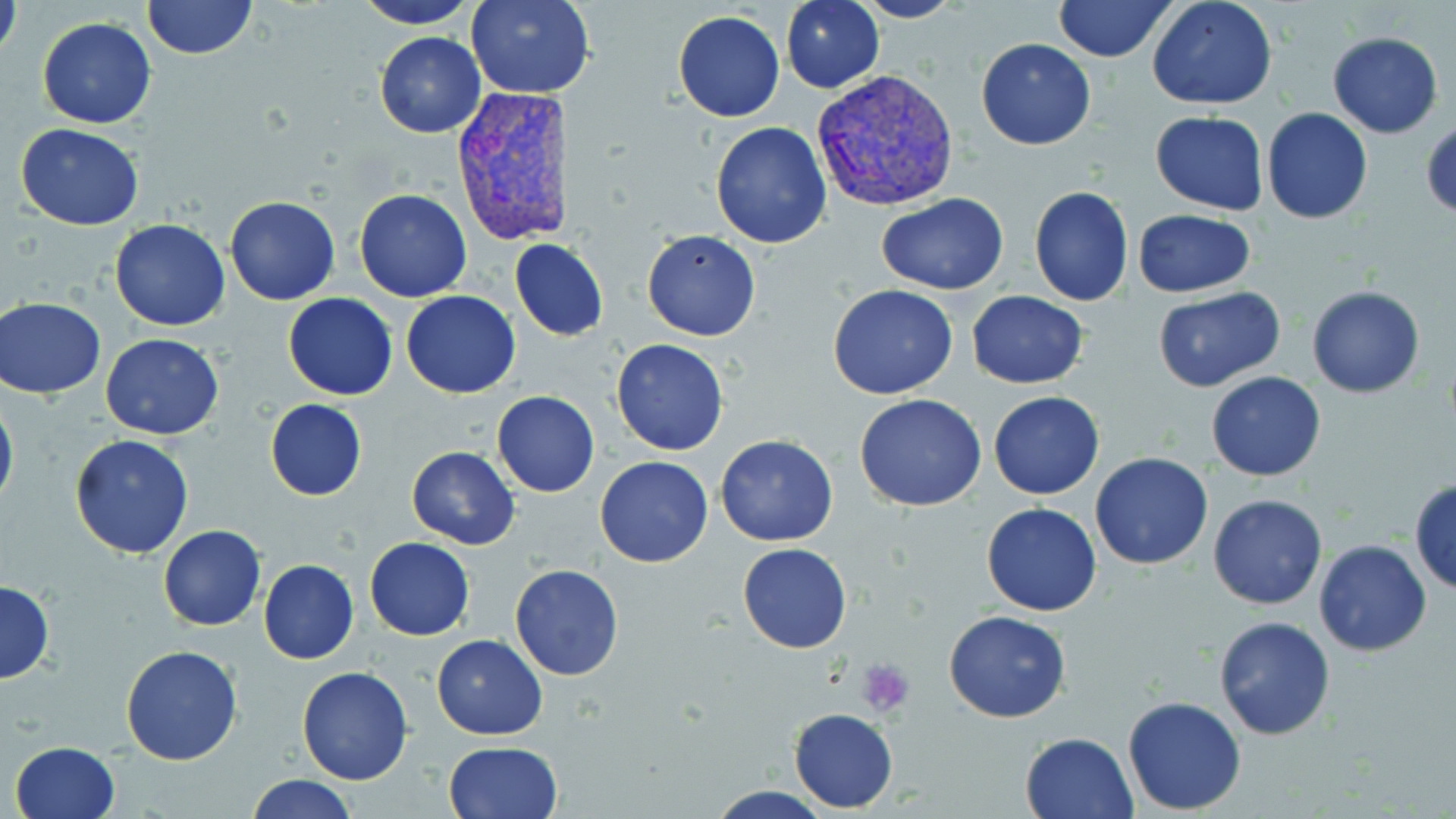

Approximate bounding boxes as (x1, y1, x2, y2) in pixels. Plasmodium vivax-infected red blood cell locations: (810, 68, 960, 213), (451, 85, 573, 244). Platelet locations: (856, 660, 916, 717). Uninfected red blood cell locations: (1, 0, 23, 69), (142, 0, 257, 59), (354, 0, 479, 28), (467, 0, 593, 98), (781, 0, 885, 93), (1147, 0, 1276, 110), (853, 1, 965, 23), (1053, 1, 1175, 62), (672, 9, 785, 122), (36, 17, 157, 129), (1327, 30, 1443, 139), (375, 32, 487, 139), (975, 38, 1097, 151), (1261, 107, 1372, 224), (1149, 110, 1269, 216), (1421, 117, 1455, 219), (711, 121, 832, 247), (16, 124, 145, 231), (1028, 185, 1134, 307), (354, 189, 472, 302), (877, 194, 1008, 293), (225, 195, 341, 305), (1133, 209, 1256, 298), (110, 218, 230, 331), (642, 230, 761, 341), (509, 237, 610, 342), (828, 284, 957, 399), (1307, 284, 1427, 398), (1153, 286, 1285, 392), (401, 289, 521, 398), (967, 291, 1088, 389), (283, 292, 398, 401), (1, 297, 107, 399), (100, 333, 225, 440), (611, 339, 728, 456), (1206, 371, 1326, 481), (492, 391, 600, 496), (988, 391, 1104, 500), (855, 393, 986, 511), (0, 394, 18, 514), (265, 399, 366, 502), (714, 433, 838, 546), (70, 434, 194, 559), (406, 446, 520, 549), (1090, 452, 1214, 569), (593, 457, 713, 569), (1409, 480, 1456, 596), (1208, 493, 1326, 609), (982, 502, 1101, 616), (158, 525, 266, 631), (363, 537, 475, 641), (1313, 539, 1432, 656), (737, 542, 851, 652), (258, 558, 360, 665), (509, 564, 626, 681), (0, 581, 54, 684), (944, 610, 1071, 724), (1212, 616, 1336, 740), (432, 633, 548, 740), (120, 643, 244, 766), (297, 665, 414, 785), (1122, 695, 1247, 816), (788, 707, 898, 812), (1020, 730, 1137, 817), (12, 741, 122, 818), (444, 741, 563, 819), (248, 774, 356, 819), (708, 786, 832, 818). Slide-level diagnosis: Plasmodium vivax. May-Grünwald-Giemsa stain. Thin blood film. Image is 1456×819 pixels. Light microscopy. Captured at 1000x magnification. One field of a larger specimen.